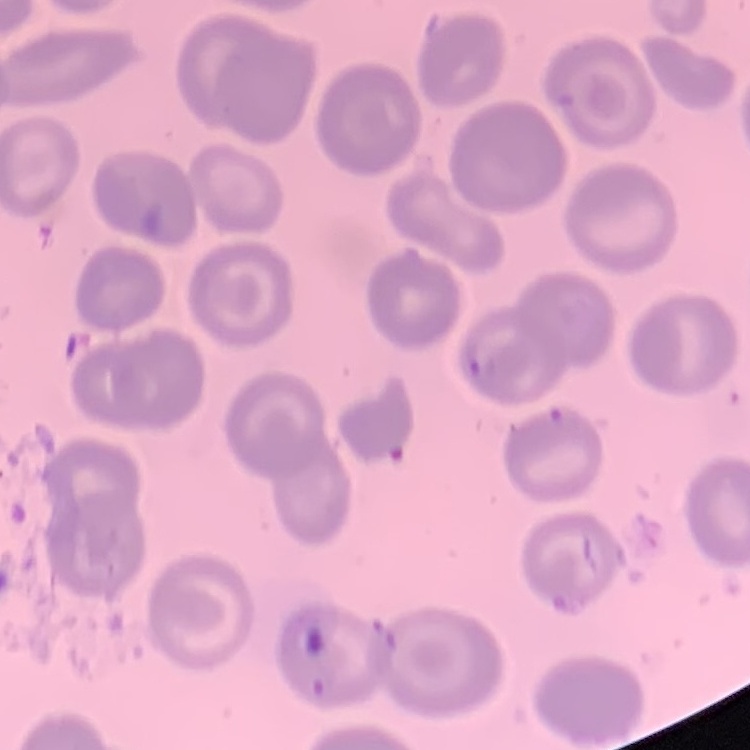
Summary:
  - Erythrocyte morphology: no rouleaux formation
  - Preparation: thin peripheral smear
  - Image type: square crop of a larger photomicrograph
  - Stain: Field's or Giemsa